Classify this cell by malaria status.
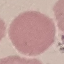

It is uninfected.

Photographed with a smartphone camera at the microscope eyepiece. Thin blood smear. Giemsa stain. Cell patch, automatically extracted from a larger field of view and resized to 64 × 64 pixels.